Name the cell type shown.
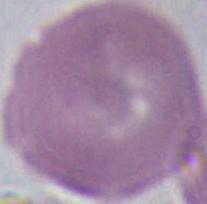
This is an erythrocyte.

modality = photomicrograph
magnification = 1000x